Report the malaria status of this cell.
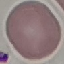
Uninfected.

stain = Giemsa
preparation = thin blood film
image type = automatically extracted cell patch, resized to 64 × 64 pixels
capture = smartphone through the microscope eyepiece